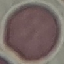
result = no malaria parasites seen
image type = automatically extracted cell patch, resized to 64 × 64 pixels
stain = Giemsa
preparation = thin blood smear
capture = smartphone camera at the microscope eyepiece